Comment on the morphology of the erythrocytes.
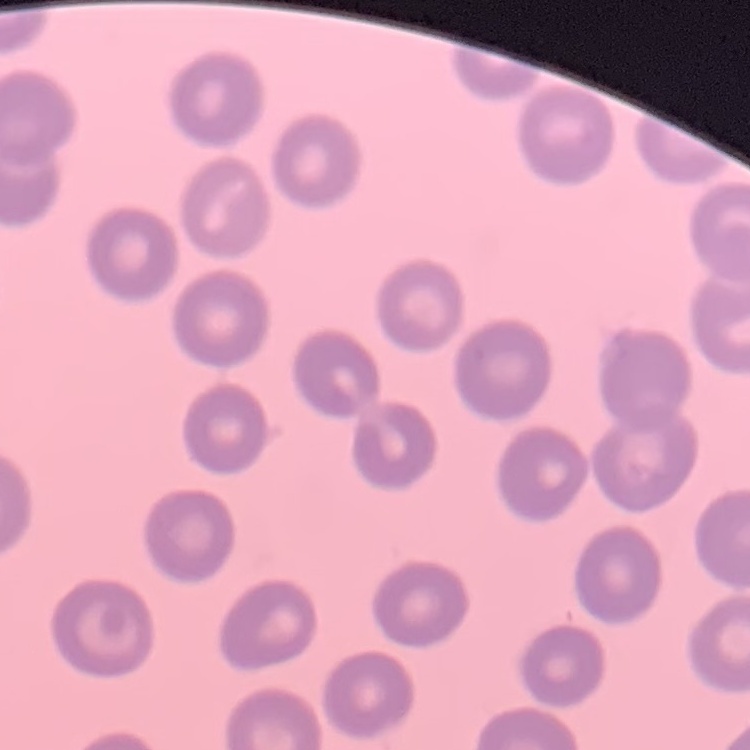

They show no rouleaux formation.

Thin peripheral smear. Field's or Giemsa stain. Square crop of a larger photomicrograph.